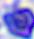

Summary:
  - Modality: photomicrograph
  - Magnification: 400x
  - Identification: white blood cell